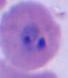
Photomicrograph. A Plasmodium parasite is shown. Captured at either 400x or 1000x magnification.